Report the malaria status of this cell.
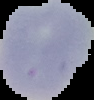

It is uninfected.

Summary:
  - Preparation: thin blood film
  - Image type: segmented cell region on a black background
  - Image size: 94×100 pixels